Describe the morphology of the erythrocytes.
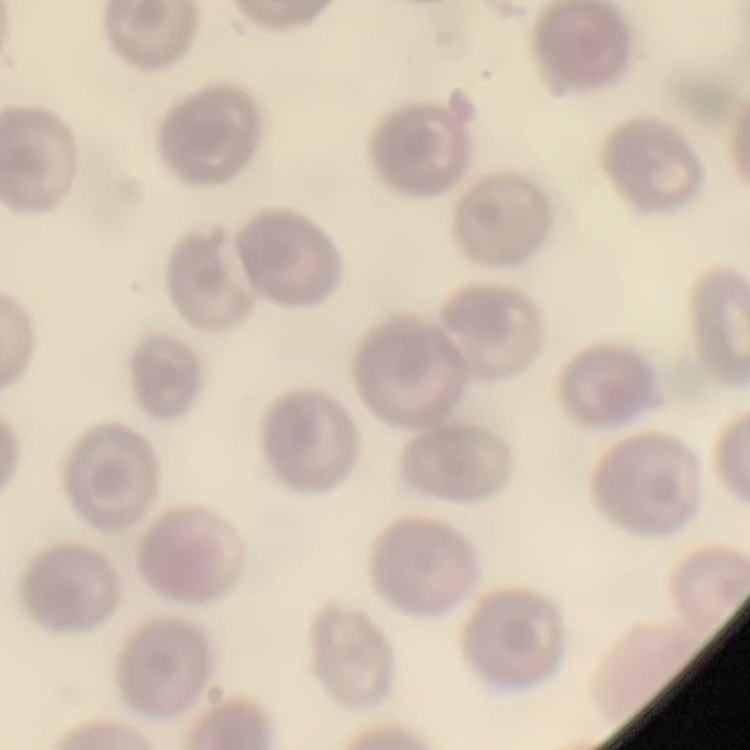
They show no rouleaux formation.

Stained with either Field's or Giemsa. Square crop of a larger photomicrograph. Thin peripheral smear.